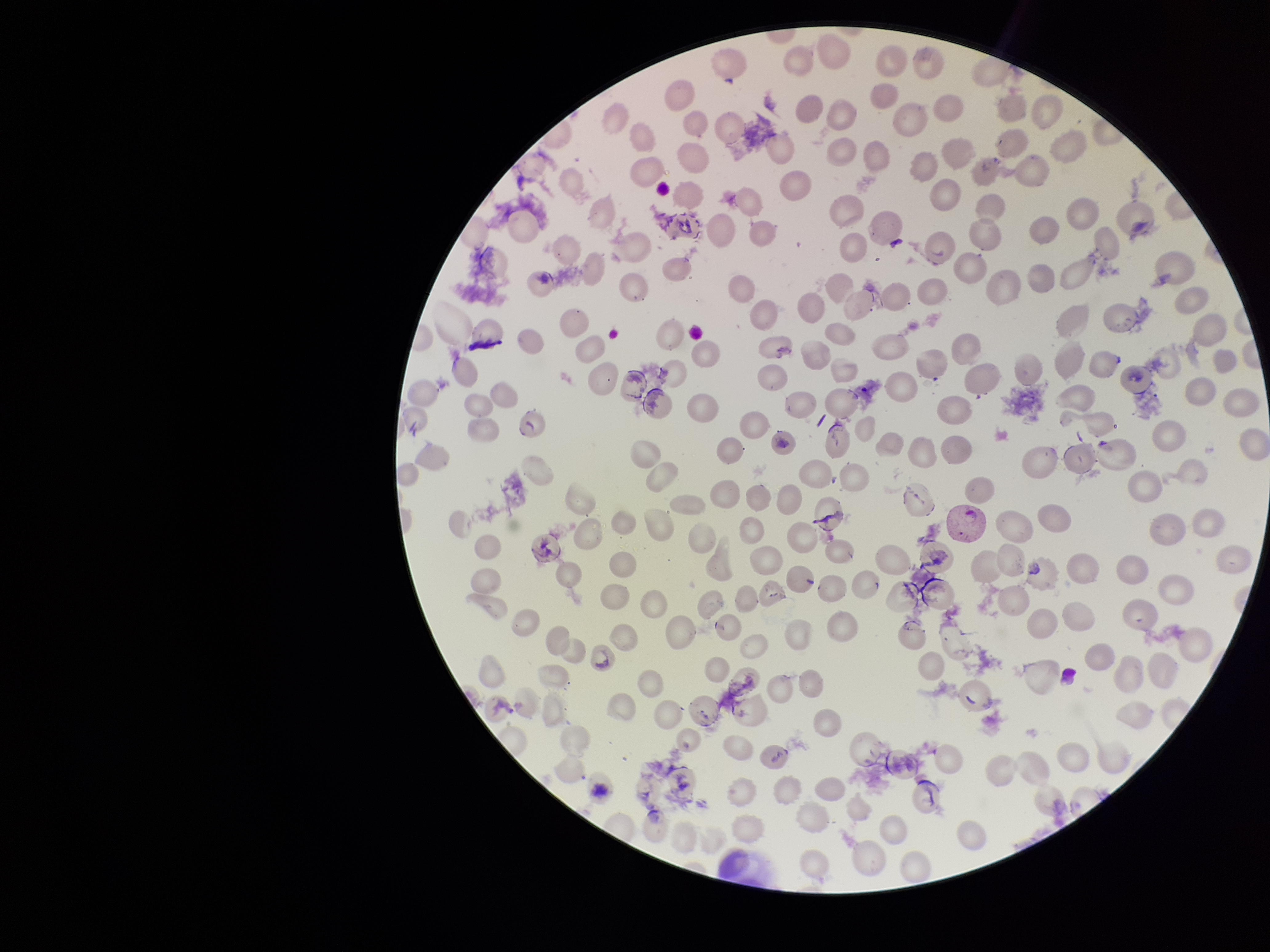
Summary:
  - Stain: Giemsa
  - Field of view: single
  - Red blood cell count: 195
  - Capture: smartphone photograph through the microscope eyepiece
  - Parasitized red blood cell count: 0
  - Patient malaria status: infected
  - Image size: 1270×952 pixels
  - Parasitized red blood cells: none seen
  - Species reported for this patient: Plasmodium vivax
  - Preparation: thin blood smear